Identify the cell.
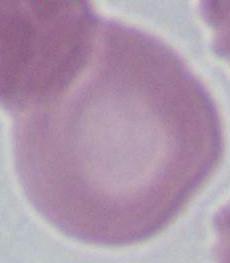
An erythrocyte.

modality: photomicrograph
magnification: 1000x